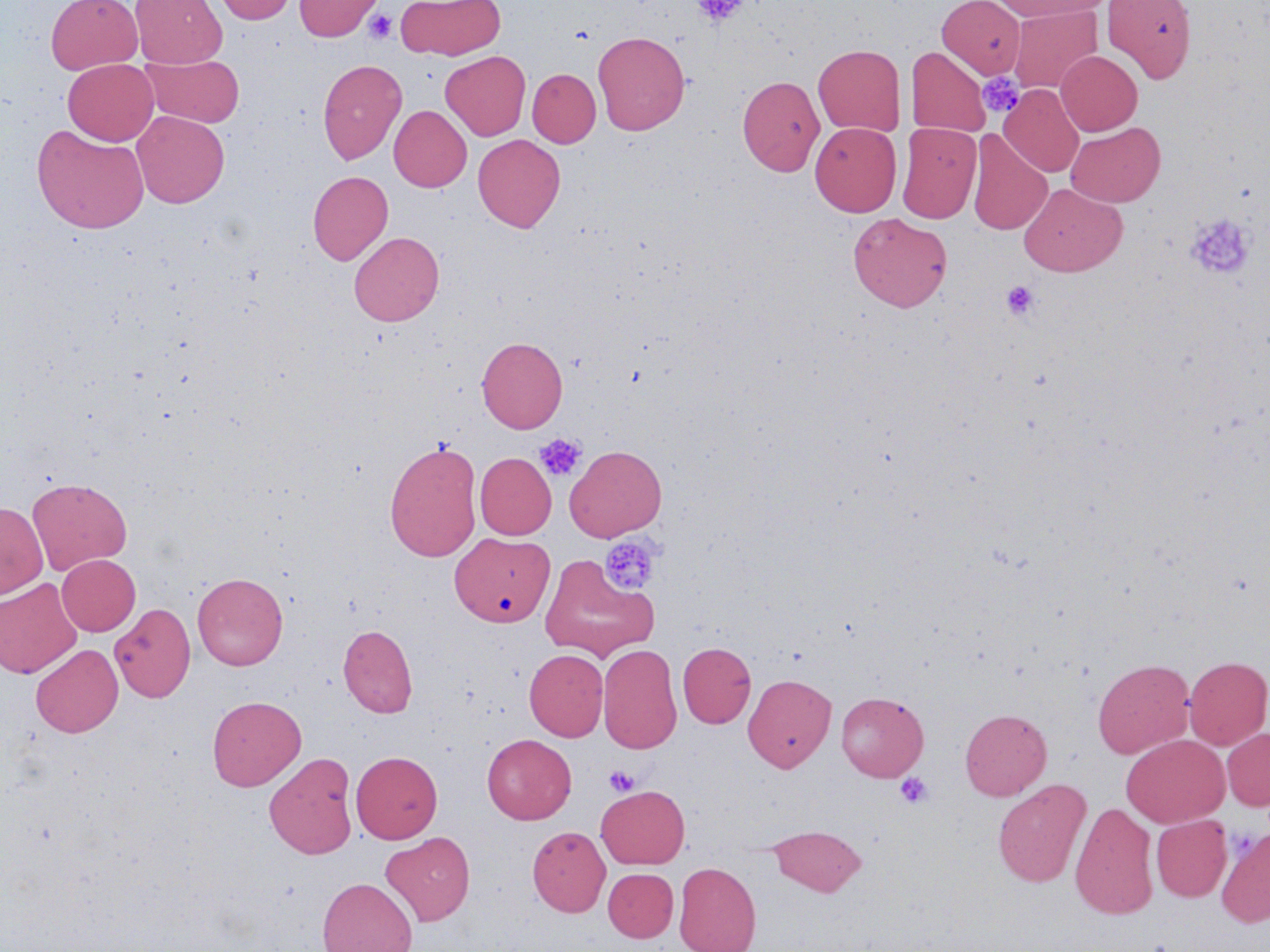 Approximate bounding boxes as named x1/y1/x2/y2 corners in pixels. Uninfected red blood cell locations (subset): (x1=46, y1=0, x2=143, y2=74), (x1=130, y1=0, x2=226, y2=67), (x1=212, y1=0, x2=299, y2=24), (x1=294, y1=0, x2=382, y2=41), (x1=395, y1=0, x2=506, y2=60), (x1=937, y1=0, x2=1025, y2=79), (x1=990, y1=0, x2=1112, y2=20), (x1=1101, y1=0, x2=1197, y2=83), (x1=1009, y1=5, x2=1102, y2=94), (x1=592, y1=30, x2=690, y2=135), (x1=813, y1=44, x2=905, y2=136), (x1=906, y1=46, x2=990, y2=137), (x1=1056, y1=50, x2=1142, y2=135), (x1=440, y1=51, x2=530, y2=141), (x1=141, y1=53, x2=245, y2=128), (x1=63, y1=59, x2=159, y2=145), (x1=318, y1=59, x2=407, y2=164), (x1=527, y1=69, x2=601, y2=147), (x1=737, y1=75, x2=825, y2=176), (x1=999, y1=84, x2=1084, y2=177), (x1=389, y1=105, x2=471, y2=192), (x1=132, y1=110, x2=229, y2=208), (x1=810, y1=122, x2=901, y2=216), (x1=1066, y1=122, x2=1165, y2=207), (x1=897, y1=123, x2=981, y2=224), (x1=32, y1=124, x2=149, y2=233), (x1=967, y1=131, x2=1052, y2=235), (x1=473, y1=134, x2=565, y2=232), (x1=307, y1=171, x2=393, y2=266), (x1=1019, y1=184, x2=1127, y2=277), (x1=848, y1=212, x2=952, y2=312), (x1=349, y1=231, x2=444, y2=326), (x1=476, y1=337, x2=567, y2=433), (x1=384, y1=441, x2=481, y2=562), (x1=565, y1=445, x2=666, y2=541), (x1=475, y1=452, x2=556, y2=539), (x1=27, y1=477, x2=132, y2=575), (x1=0, y1=502, x2=48, y2=598), (x1=453, y1=533, x2=557, y2=629), (x1=57, y1=554, x2=140, y2=635), (x1=192, y1=572, x2=288, y2=670), (x1=0, y1=578, x2=82, y2=678), (x1=110, y1=602, x2=196, y2=702), (x1=338, y1=624, x2=418, y2=718), (x1=677, y1=642, x2=756, y2=728), (x1=31, y1=644, x2=123, y2=737), (x1=598, y1=644, x2=682, y2=754), (x1=524, y1=649, x2=608, y2=741), (x1=1183, y1=656, x2=1270, y2=750), (x1=1092, y1=658, x2=1194, y2=759), (x1=743, y1=674, x2=836, y2=772), (x1=836, y1=692, x2=928, y2=781), (x1=207, y1=695, x2=306, y2=790), (x1=960, y1=708, x2=1052, y2=800), (x1=1221, y1=727, x2=1270, y2=811), (x1=482, y1=734, x2=576, y2=824), (x1=1121, y1=734, x2=1229, y2=827), (x1=351, y1=751, x2=442, y2=843), (x1=264, y1=752, x2=358, y2=859), (x1=993, y1=779, x2=1091, y2=888), (x1=596, y1=785, x2=689, y2=868), (x1=1069, y1=801, x2=1159, y2=920), (x1=1151, y1=816, x2=1231, y2=901), (x1=527, y1=825, x2=611, y2=917), (x1=769, y1=825, x2=866, y2=896), (x1=1217, y1=827, x2=1270, y2=926), (x1=380, y1=831, x2=476, y2=926), (x1=674, y1=861, x2=761, y2=952), (x1=603, y1=868, x2=678, y2=942), (x1=317, y1=877, x2=418, y2=952). Platelet locations (subset): (x1=692, y1=0, x2=750, y2=26), (x1=363, y1=9, x2=398, y2=44), (x1=977, y1=72, x2=1025, y2=119), (x1=1186, y1=213, x2=1254, y2=279), (x1=1001, y1=281, x2=1039, y2=321), (x1=534, y1=433, x2=586, y2=481), (x1=599, y1=534, x2=661, y2=596), (x1=604, y1=766, x2=639, y2=796), (x1=895, y1=772, x2=932, y2=808). Slide-level diagnosis: no evidence of blood parasites. Captured at 1000x magnification. One field of a larger specimen. Optical microscopy. Image is 1270×952 pixels. May-Grünwald-Giemsa stain. Thin blood film.